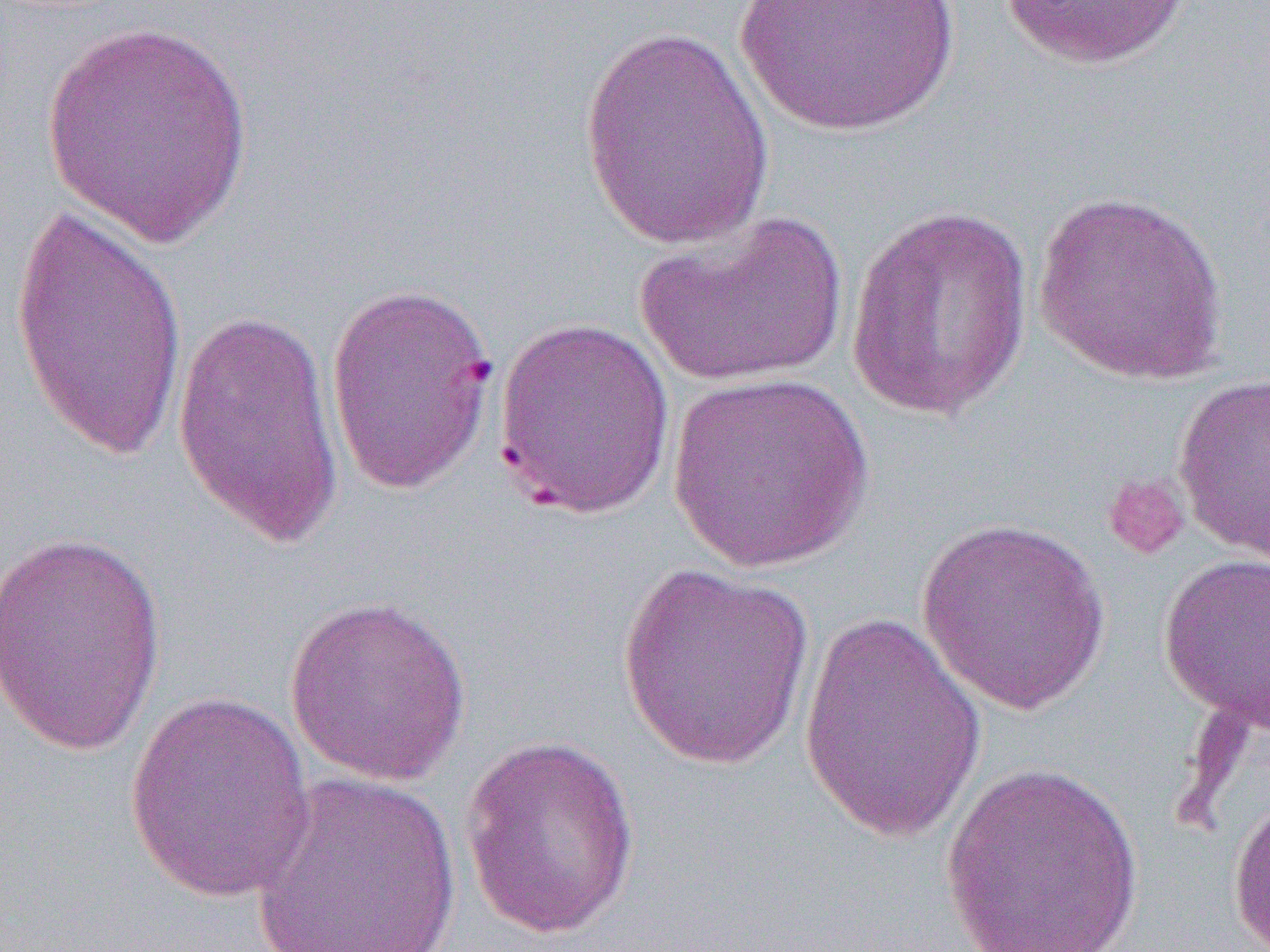

Summary:
  - Coordinate format: approximate bounding boxes as named x1/y1/x2/y2 corners in pixels
  - Platelet locations: (x1=1101, y1=472, x2=1190, y2=560)
  - Uninfected red blood cell locations: (x1=733, y1=0, x2=962, y2=141), (x1=996, y1=0, x2=1195, y2=72), (x1=40, y1=17, x2=256, y2=249), (x1=576, y1=23, x2=775, y2=251), (x1=1032, y1=188, x2=1231, y2=386), (x1=10, y1=195, x2=189, y2=465), (x1=845, y1=204, x2=1034, y2=422), (x1=635, y1=211, x2=848, y2=389), (x1=324, y1=279, x2=500, y2=499), (x1=170, y1=305, x2=345, y2=553), (x1=492, y1=317, x2=677, y2=521), (x1=663, y1=370, x2=876, y2=573), (x1=1172, y1=373, x2=1270, y2=564), (x1=915, y1=516, x2=1112, y2=715), (x1=0, y1=528, x2=168, y2=759), (x1=1157, y1=552, x2=1270, y2=731), (x1=617, y1=562, x2=816, y2=771), (x1=282, y1=594, x2=473, y2=786), (x1=797, y1=609, x2=989, y2=847), (x1=123, y1=690, x2=318, y2=905), (x1=459, y1=735, x2=641, y2=939), (x1=940, y1=761, x2=1146, y2=952), (x1=251, y1=772, x2=462, y2=951), (x1=1227, y1=786, x2=1270, y2=950)
  - Slide-level diagnosis: Plasmodium falciparum
  - Modality: optical microscopy
  - Preparation: thin blood smear
  - Image size: 1270×952 pixels
  - Magnification: 1000x
  - Field of view: single